Give the location of every parasitized RBC.
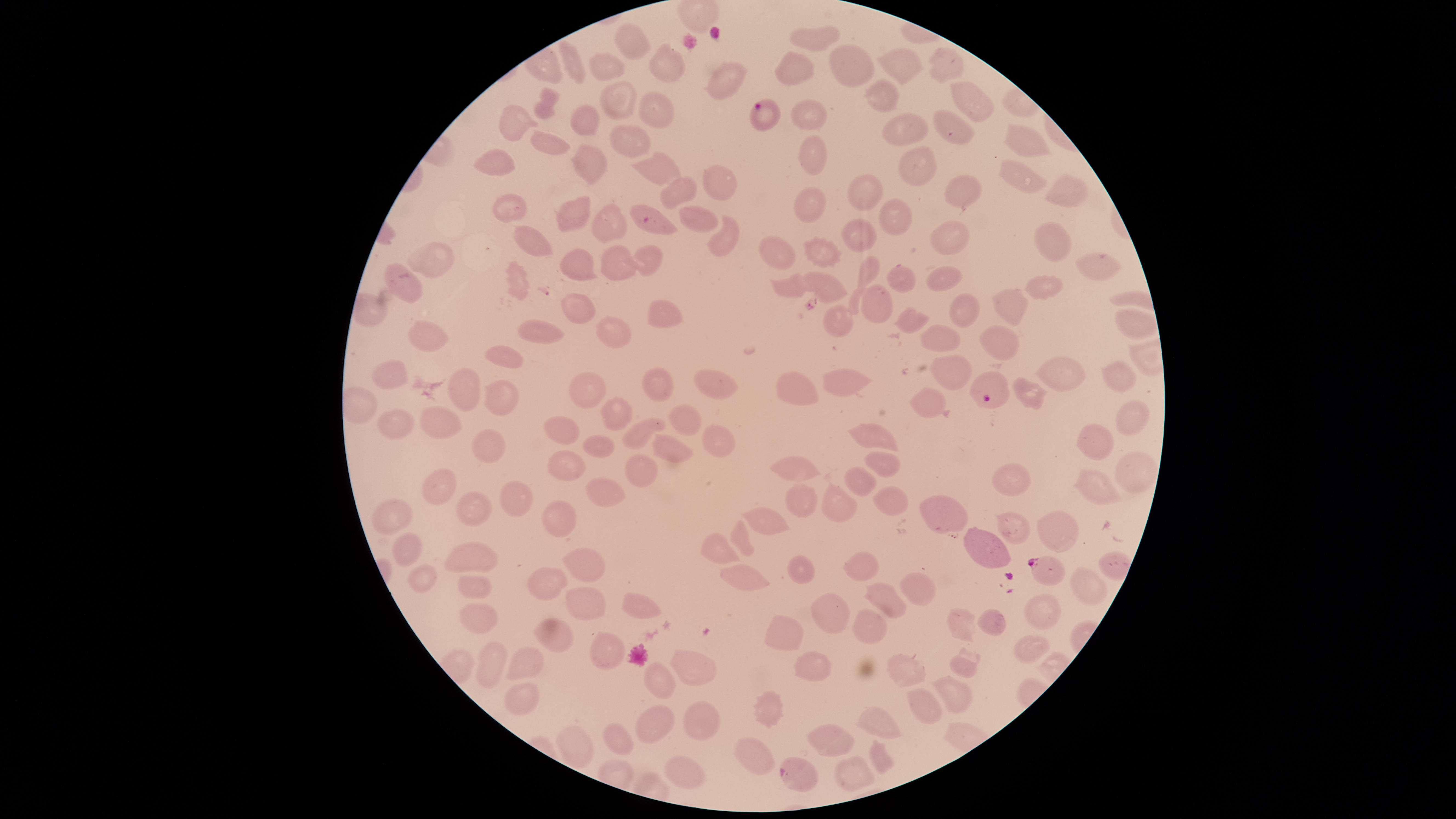
Approximate bounding boxes, in pixels from the top-left corner.
Parasitized RBCs: (left=750, top=99, right=781, bottom=132), (left=629, top=205, right=678, bottom=235), (left=968, top=371, right=1010, bottom=409), (left=1028, top=556, right=1066, bottom=587), (left=780, top=757, right=818, bottom=793).

Approximate bounding boxes, in pixels from the top-left corner.
Summary:
  - Uninfected RBCs: (left=613, top=22, right=653, bottom=60), (left=789, top=26, right=839, bottom=51), (left=558, top=40, right=586, bottom=85), (left=647, top=41, right=687, bottom=82), (left=828, top=44, right=875, bottom=88), (left=876, top=47, right=926, bottom=85), (left=928, top=47, right=964, bottom=85), (left=588, top=50, right=625, bottom=81), (left=774, top=50, right=816, bottom=86), (left=703, top=60, right=748, bottom=101), (left=865, top=78, right=900, bottom=113), (left=599, top=79, right=636, bottom=121), (left=948, top=79, right=994, bottom=122), (left=533, top=87, right=559, bottom=119), (left=637, top=91, right=674, bottom=129), (left=789, top=99, right=828, bottom=131), (left=499, top=104, right=539, bottom=142), (left=569, top=104, right=600, bottom=136), (left=933, top=109, right=975, bottom=145), (left=880, top=113, right=929, bottom=147), (left=1002, top=121, right=1053, bottom=157), (left=609, top=124, right=652, bottom=159), (left=531, top=130, right=571, bottom=155), (left=798, top=135, right=826, bottom=177), (left=570, top=143, right=608, bottom=184), (left=898, top=146, right=937, bottom=186), (left=473, top=147, right=517, bottom=176), (left=630, top=150, right=683, bottom=187), (left=997, top=158, right=1047, bottom=194), (left=701, top=165, right=737, bottom=200), (left=846, top=173, right=883, bottom=211), (left=1043, top=173, right=1090, bottom=209), (left=658, top=175, right=697, bottom=210), (left=945, top=175, right=982, bottom=207), (left=793, top=187, right=827, bottom=223), (left=494, top=192, right=527, bottom=224), (left=555, top=196, right=590, bottom=233), (left=878, top=199, right=912, bottom=236), (left=591, top=203, right=628, bottom=243), (left=677, top=206, right=719, bottom=233), (left=707, top=214, right=740, bottom=257), (left=840, top=218, right=877, bottom=253), (left=931, top=220, right=971, bottom=256), (left=1035, top=221, right=1072, bottom=262), (left=514, top=225, right=554, bottom=256), (left=758, top=235, right=798, bottom=269), (left=802, top=236, right=843, bottom=269), (left=406, top=242, right=455, bottom=279), (left=600, top=244, right=641, bottom=281), (left=623, top=245, right=662, bottom=275), (left=558, top=248, right=599, bottom=281), (left=1073, top=252, right=1123, bottom=281), (left=847, top=255, right=880, bottom=315), (left=505, top=259, right=530, bottom=301), (left=384, top=261, right=423, bottom=305), (left=926, top=264, right=961, bottom=292), (left=886, top=265, right=916, bottom=293), (left=803, top=271, right=847, bottom=302), (left=769, top=273, right=806, bottom=297), (left=1023, top=275, right=1064, bottom=301), (left=860, top=285, right=894, bottom=324), (left=992, top=289, right=1029, bottom=326), (left=949, top=291, right=980, bottom=328), (left=561, top=292, right=595, bottom=325), (left=646, top=299, right=684, bottom=328), (left=822, top=304, right=854, bottom=338), (left=894, top=307, right=930, bottom=334), (left=1116, top=307, right=1158, bottom=340), (left=596, top=315, right=632, bottom=348), (left=408, top=319, right=450, bottom=351), (left=517, top=319, right=565, bottom=343), (left=919, top=323, right=961, bottom=352), (left=978, top=324, right=1019, bottom=361), (left=484, top=344, right=524, bottom=369), (left=929, top=354, right=972, bottom=390), (left=1037, top=356, right=1086, bottom=392), (left=372, top=359, right=408, bottom=390), (left=1101, top=360, right=1137, bottom=392), (left=641, top=365, right=675, bottom=402), (left=445, top=367, right=481, bottom=411), (left=822, top=368, right=871, bottom=397), (left=568, top=370, right=607, bottom=410), (left=693, top=370, right=740, bottom=399), (left=775, top=371, right=819, bottom=406), (left=1012, top=376, right=1048, bottom=411), (left=483, top=379, right=518, bottom=416), (left=908, top=387, right=946, bottom=418), (left=601, top=397, right=632, bottom=431), (left=1114, top=399, right=1150, bottom=437), (left=668, top=404, right=702, bottom=435), (left=418, top=407, right=464, bottom=438), (left=376, top=408, right=415, bottom=441), (left=544, top=416, right=581, bottom=444), (left=621, top=419, right=667, bottom=450), (left=700, top=423, right=735, bottom=459), (left=1076, top=423, right=1116, bottom=461), (left=847, top=424, right=900, bottom=453), (left=471, top=427, right=505, bottom=464), (left=650, top=433, right=693, bottom=463), (left=583, top=434, right=615, bottom=458), (left=547, top=449, right=587, bottom=482), (left=864, top=451, right=901, bottom=478), (left=1113, top=451, right=1158, bottom=494), (left=624, top=452, right=658, bottom=487), (left=769, top=456, right=824, bottom=482), (left=992, top=463, right=1031, bottom=497), (left=843, top=466, right=877, bottom=496), (left=421, top=468, right=456, bottom=505), (left=1074, top=468, right=1123, bottom=506), (left=585, top=477, right=627, bottom=508), (left=499, top=481, right=532, bottom=517), (left=821, top=481, right=859, bottom=523), (left=785, top=483, right=818, bottom=518), (left=872, top=487, right=910, bottom=516), (left=456, top=491, right=493, bottom=525), (left=919, top=495, right=967, bottom=537), (left=371, top=498, right=413, bottom=534), (left=541, top=500, right=576, bottom=537), (left=743, top=506, right=792, bottom=536), (left=1036, top=510, right=1080, bottom=552), (left=994, top=511, right=1031, bottom=546), (left=729, top=518, right=755, bottom=557), (left=963, top=527, right=1012, bottom=569), (left=392, top=532, right=422, bottom=567), (left=700, top=532, right=740, bottom=565), (left=444, top=541, right=499, bottom=574), (left=560, top=546, right=606, bottom=582), (left=842, top=550, right=879, bottom=581), (left=1098, top=550, right=1132, bottom=580), (left=787, top=555, right=816, bottom=584), (left=406, top=563, right=437, bottom=593), (left=720, top=564, right=770, bottom=591), (left=1068, top=566, right=1107, bottom=606), (left=527, top=567, right=568, bottom=601), (left=899, top=571, right=936, bottom=606), (left=456, top=575, right=492, bottom=600), (left=863, top=581, right=907, bottom=619), (left=565, top=587, right=605, bottom=620), (left=620, top=592, right=662, bottom=619), (left=811, top=593, right=850, bottom=634), (left=1024, top=594, right=1062, bottom=630), (left=459, top=602, right=500, bottom=634), (left=851, top=608, right=887, bottom=645), (left=947, top=608, right=976, bottom=643), (left=978, top=608, right=1007, bottom=636), (left=763, top=614, right=803, bottom=651), (left=533, top=617, right=575, bottom=653), (left=589, top=631, right=625, bottom=670), (left=1013, top=634, right=1051, bottom=663), (left=476, top=641, right=508, bottom=689), (left=506, top=646, right=544, bottom=680), (left=949, top=648, right=981, bottom=678), (left=669, top=649, right=716, bottom=686), (left=793, top=650, right=832, bottom=682), (left=885, top=652, right=926, bottom=686), (left=644, top=661, right=676, bottom=700), (left=930, top=675, right=972, bottom=714), (left=502, top=680, right=539, bottom=716), (left=906, top=688, right=943, bottom=724), (left=752, top=690, right=784, bottom=729), (left=681, top=700, right=720, bottom=740), (left=635, top=705, right=675, bottom=742), (left=855, top=706, right=901, bottom=739), (left=806, top=723, right=855, bottom=756), (left=603, top=724, right=634, bottom=755), (left=555, top=726, right=594, bottom=769), (left=732, top=737, right=776, bottom=775), (left=868, top=739, right=894, bottom=774), (left=832, top=754, right=875, bottom=791), (left=663, top=755, right=705, bottom=789)
  - Capture: smartphone photograph through the microscope eyepiece
  - Stain: Giemsa
  - Visible region: circular
  - Field of view: single
  - Image size: 1456×819 pixels
  - Preparation: thin blood film
  - Species: Plasmodium falciparum